Report the malaria status of this cell.
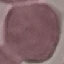
Uninfected.

image type = automatically extracted cell patch, resized to 64 × 64 pixels
stain = Giemsa
preparation = thin smear
capture = smartphone camera at the microscope eyepiece